Locate every leukocyte (white blood cell).
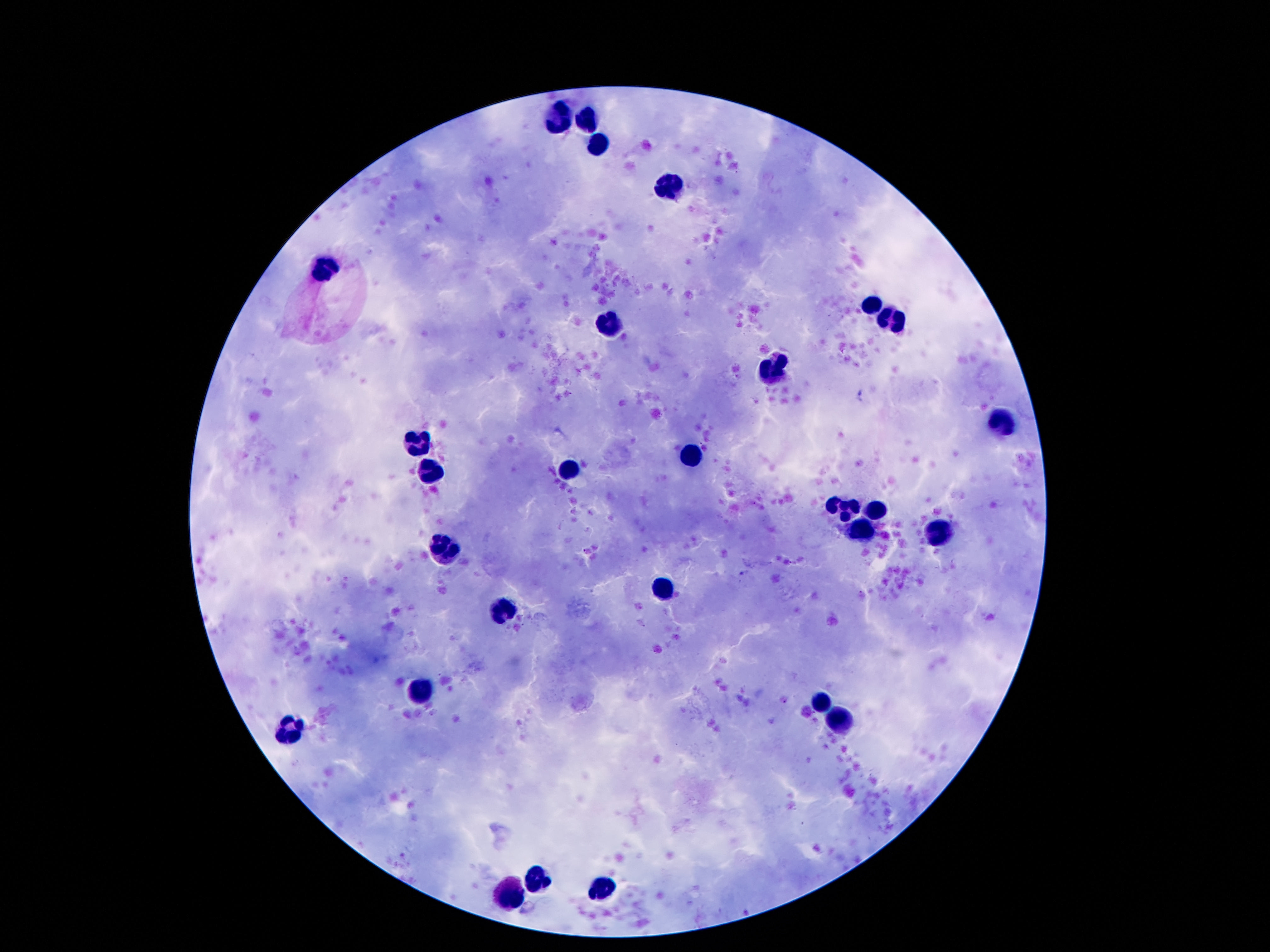
Approximate centers as {x, y} in pixels.
Leukocytes: {565, 113}, {586, 115}, {595, 144}, {672, 189}, {322, 262}, {874, 305}, {890, 319}, {606, 324}, {776, 371}, {1003, 424}, {422, 439}, {692, 455}, {567, 469}, {434, 471}, {847, 507}, {878, 507}, {863, 528}, {940, 530}, {447, 548}, {661, 589}, {502, 610}, {422, 689}, {822, 698}, {842, 723}, {288, 728}, {538, 880}, {602, 889}, {504, 895}.

image_size: 1270×952 pixels
capture: smartphone camera through the microscope eyepiece
magnification: 100x
patient_malaria_status: not infected
field_of_view: one from this slide
stain: Giemsa
preparation: thick blood smear